Describe the morphology of the red blood cells.
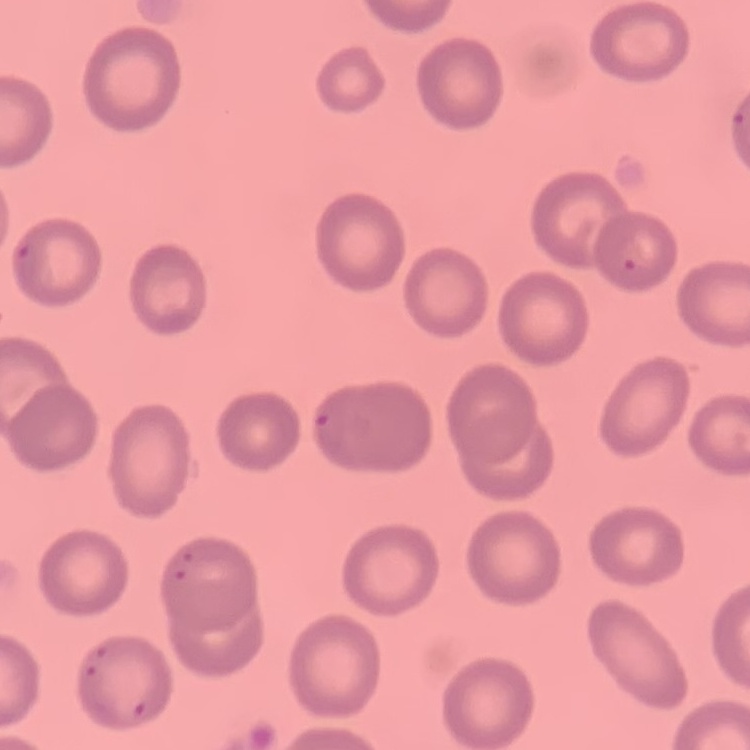
They show no rouleaux formation.

Summary:
  - Stain: Field's or Giemsa
  - Image type: one tile cut from a larger photomicrograph
  - Preparation: thin blood film